Mark where platelets are.
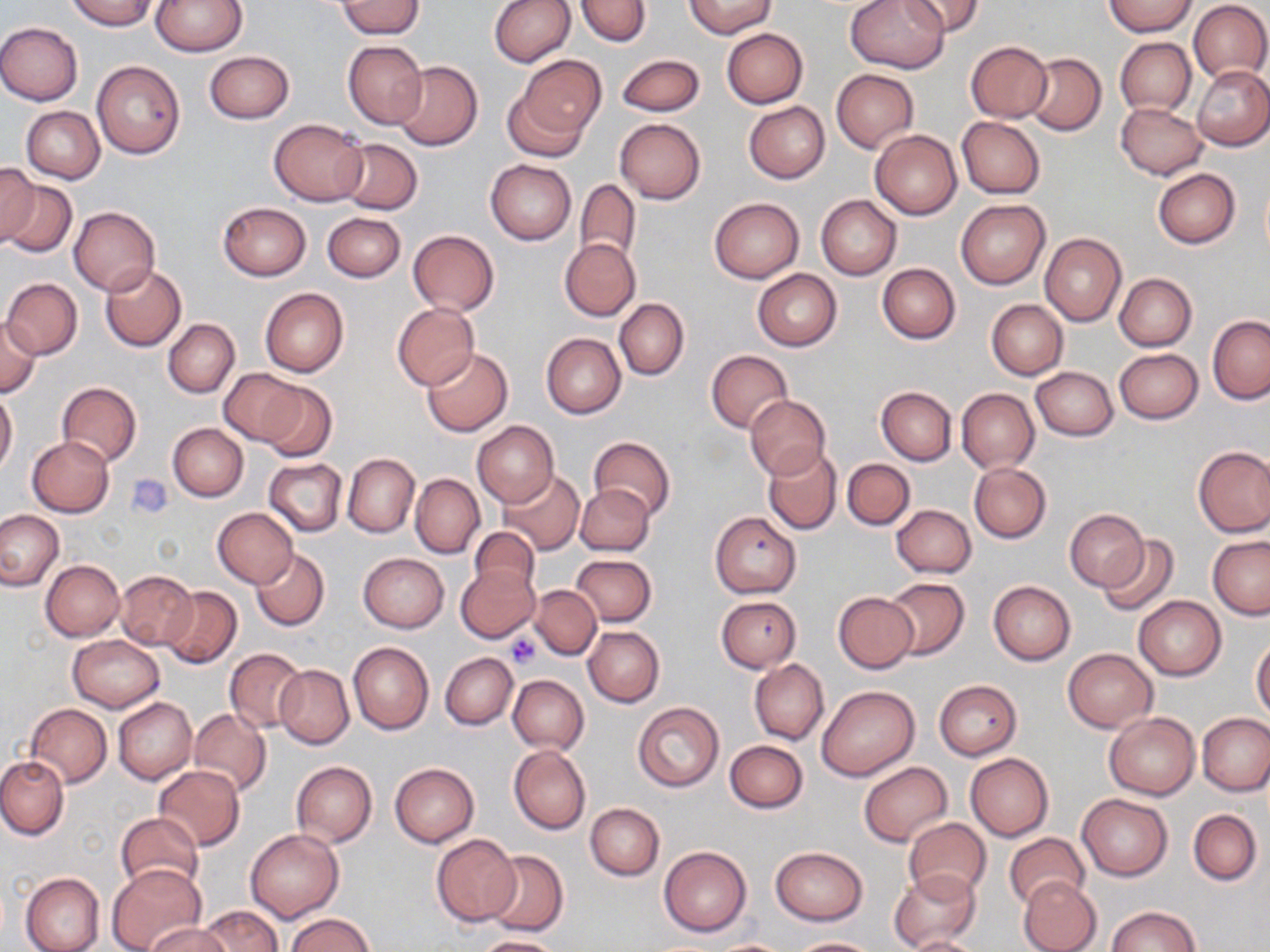
Approximate bounding boxes as named x1/y1/x2/y2 corners in pixels.
Platelets: (x1=504, y1=631, x2=543, y2=669).

slide-level diagnosis = no evidence of blood parasites
image size = 1270×952 pixels
stain = May-Grünwald-Giemsa
magnification = 1000x
preparation = thin blood smear
modality = light microscopy
uninfected red blood cell locations = approximate bounding boxes as named x1/y1/x2/y2 corners in pixels: (x1=67, y1=0, x2=159, y2=31), (x1=152, y1=0, x2=246, y2=55), (x1=488, y1=0, x2=575, y2=67), (x1=576, y1=0, x2=650, y2=47), (x1=685, y1=0, x2=776, y2=38), (x1=846, y1=0, x2=949, y2=73), (x1=903, y1=0, x2=984, y2=38), (x1=1187, y1=0, x2=1270, y2=83), (x1=336, y1=2, x2=425, y2=38), (x1=1104, y1=2, x2=1198, y2=37), (x1=0, y1=21, x2=82, y2=105), (x1=722, y1=28, x2=807, y2=108), (x1=1115, y1=38, x2=1196, y2=116), (x1=342, y1=41, x2=428, y2=129), (x1=966, y1=42, x2=1052, y2=122), (x1=203, y1=51, x2=295, y2=124), (x1=1024, y1=52, x2=1106, y2=135), (x1=518, y1=55, x2=605, y2=142), (x1=616, y1=55, x2=705, y2=117), (x1=391, y1=60, x2=483, y2=151), (x1=92, y1=61, x2=185, y2=159), (x1=1193, y1=65, x2=1270, y2=151), (x1=831, y1=69, x2=918, y2=151), (x1=501, y1=82, x2=594, y2=164), (x1=744, y1=101, x2=830, y2=184), (x1=1116, y1=103, x2=1207, y2=179), (x1=21, y1=106, x2=105, y2=183), (x1=957, y1=117, x2=1045, y2=198), (x1=268, y1=118, x2=368, y2=205), (x1=615, y1=118, x2=706, y2=203), (x1=870, y1=129, x2=962, y2=220), (x1=337, y1=138, x2=423, y2=214), (x1=485, y1=159, x2=577, y2=245), (x1=0, y1=164, x2=38, y2=247), (x1=1152, y1=168, x2=1240, y2=248), (x1=2, y1=178, x2=77, y2=260), (x1=574, y1=180, x2=640, y2=266), (x1=816, y1=195, x2=901, y2=279), (x1=710, y1=198, x2=804, y2=282), (x1=956, y1=199, x2=1050, y2=289), (x1=218, y1=202, x2=311, y2=281), (x1=69, y1=207, x2=160, y2=295), (x1=322, y1=212, x2=405, y2=283), (x1=407, y1=230, x2=499, y2=315), (x1=1040, y1=234, x2=1126, y2=326), (x1=559, y1=239, x2=640, y2=321), (x1=99, y1=263, x2=187, y2=352), (x1=878, y1=263, x2=959, y2=343), (x1=753, y1=269, x2=841, y2=351), (x1=1114, y1=273, x2=1196, y2=351), (x1=3, y1=278, x2=82, y2=358), (x1=260, y1=288, x2=348, y2=377), (x1=614, y1=299, x2=688, y2=379), (x1=986, y1=299, x2=1068, y2=380), (x1=392, y1=304, x2=479, y2=389), (x1=0, y1=314, x2=42, y2=398), (x1=1208, y1=315, x2=1269, y2=404), (x1=163, y1=318, x2=240, y2=397), (x1=541, y1=334, x2=625, y2=418), (x1=422, y1=347, x2=513, y2=437), (x1=1114, y1=349, x2=1203, y2=424), (x1=706, y1=350, x2=793, y2=432), (x1=219, y1=367, x2=308, y2=446), (x1=1030, y1=367, x2=1118, y2=440), (x1=255, y1=380, x2=337, y2=461), (x1=57, y1=382, x2=141, y2=466), (x1=876, y1=385, x2=956, y2=465), (x1=956, y1=388, x2=1039, y2=472), (x1=0, y1=390, x2=17, y2=475), (x1=743, y1=395, x2=832, y2=479), (x1=472, y1=421, x2=557, y2=507), (x1=168, y1=422, x2=248, y2=502), (x1=26, y1=436, x2=113, y2=518), (x1=589, y1=436, x2=676, y2=522), (x1=1193, y1=444, x2=1270, y2=537), (x1=763, y1=446, x2=842, y2=535), (x1=343, y1=453, x2=418, y2=538), (x1=842, y1=458, x2=915, y2=531), (x1=265, y1=459, x2=346, y2=535), (x1=969, y1=463, x2=1052, y2=543), (x1=497, y1=470, x2=587, y2=555), (x1=411, y1=474, x2=484, y2=558), (x1=575, y1=484, x2=654, y2=557), (x1=891, y1=503, x2=976, y2=577), (x1=212, y1=507, x2=298, y2=588), (x1=1, y1=509, x2=64, y2=591), (x1=1067, y1=510, x2=1148, y2=591), (x1=711, y1=511, x2=802, y2=598), (x1=468, y1=526, x2=541, y2=599), (x1=1096, y1=536, x2=1180, y2=618), (x1=1208, y1=536, x2=1270, y2=619), (x1=252, y1=548, x2=330, y2=631), (x1=357, y1=552, x2=449, y2=632), (x1=572, y1=554, x2=656, y2=626), (x1=41, y1=560, x2=123, y2=641), (x1=456, y1=565, x2=540, y2=642), (x1=117, y1=570, x2=197, y2=649), (x1=882, y1=577, x2=970, y2=661), (x1=989, y1=580, x2=1075, y2=665), (x1=531, y1=585, x2=600, y2=660), (x1=160, y1=586, x2=242, y2=669), (x1=834, y1=591, x2=919, y2=672), (x1=716, y1=595, x2=801, y2=672), (x1=1133, y1=596, x2=1226, y2=681), (x1=583, y1=626, x2=664, y2=707), (x1=68, y1=635, x2=164, y2=712), (x1=1251, y1=637, x2=1270, y2=721), (x1=348, y1=641, x2=433, y2=734), (x1=225, y1=648, x2=308, y2=732), (x1=1062, y1=648, x2=1158, y2=732), (x1=441, y1=652, x2=518, y2=730), (x1=750, y1=659, x2=828, y2=745), (x1=274, y1=664, x2=354, y2=749), (x1=507, y1=675, x2=588, y2=754), (x1=933, y1=680, x2=1022, y2=759), (x1=816, y1=684, x2=920, y2=781), (x1=113, y1=697, x2=197, y2=785), (x1=632, y1=702, x2=724, y2=792), (x1=26, y1=703, x2=112, y2=787), (x1=188, y1=709, x2=271, y2=795), (x1=1104, y1=712, x2=1200, y2=799), (x1=1196, y1=713, x2=1270, y2=797), (x1=725, y1=739, x2=807, y2=813), (x1=509, y1=746, x2=590, y2=834), (x1=965, y1=753, x2=1054, y2=842), (x1=0, y1=754, x2=68, y2=840), (x1=291, y1=762, x2=377, y2=846), (x1=389, y1=762, x2=479, y2=847), (x1=858, y1=762, x2=953, y2=847), (x1=153, y1=764, x2=245, y2=850), (x1=1076, y1=793, x2=1173, y2=880), (x1=585, y1=803, x2=664, y2=880), (x1=1188, y1=809, x2=1261, y2=885), (x1=116, y1=812, x2=203, y2=895), (x1=903, y1=818, x2=992, y2=902), (x1=246, y1=829, x2=343, y2=922), (x1=1005, y1=832, x2=1088, y2=910), (x1=431, y1=833, x2=521, y2=926), (x1=659, y1=846, x2=751, y2=937), (x1=771, y1=846, x2=868, y2=925), (x1=483, y1=850, x2=568, y2=937), (x1=107, y1=862, x2=206, y2=952), (x1=889, y1=868, x2=981, y2=951), (x1=20, y1=872, x2=104, y2=952), (x1=1018, y1=875, x2=1101, y2=952), (x1=198, y1=905, x2=283, y2=952), (x1=1106, y1=906, x2=1200, y2=951), (x1=284, y1=913, x2=374, y2=951), (x1=144, y1=923, x2=233, y2=952), (x1=473, y1=935, x2=562, y2=952), (x1=908, y1=935, x2=982, y2=952), (x1=789, y1=937, x2=878, y2=951), (x1=709, y1=939, x2=794, y2=951)
field of view = single